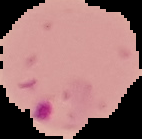
Summary:
  - Image size: 142×139 pixels
  - Image type: segmented cell region on a black background
  - Preparation: thin blood smear
  - Result: Plasmodium parasites identified